Identify the preparation type.
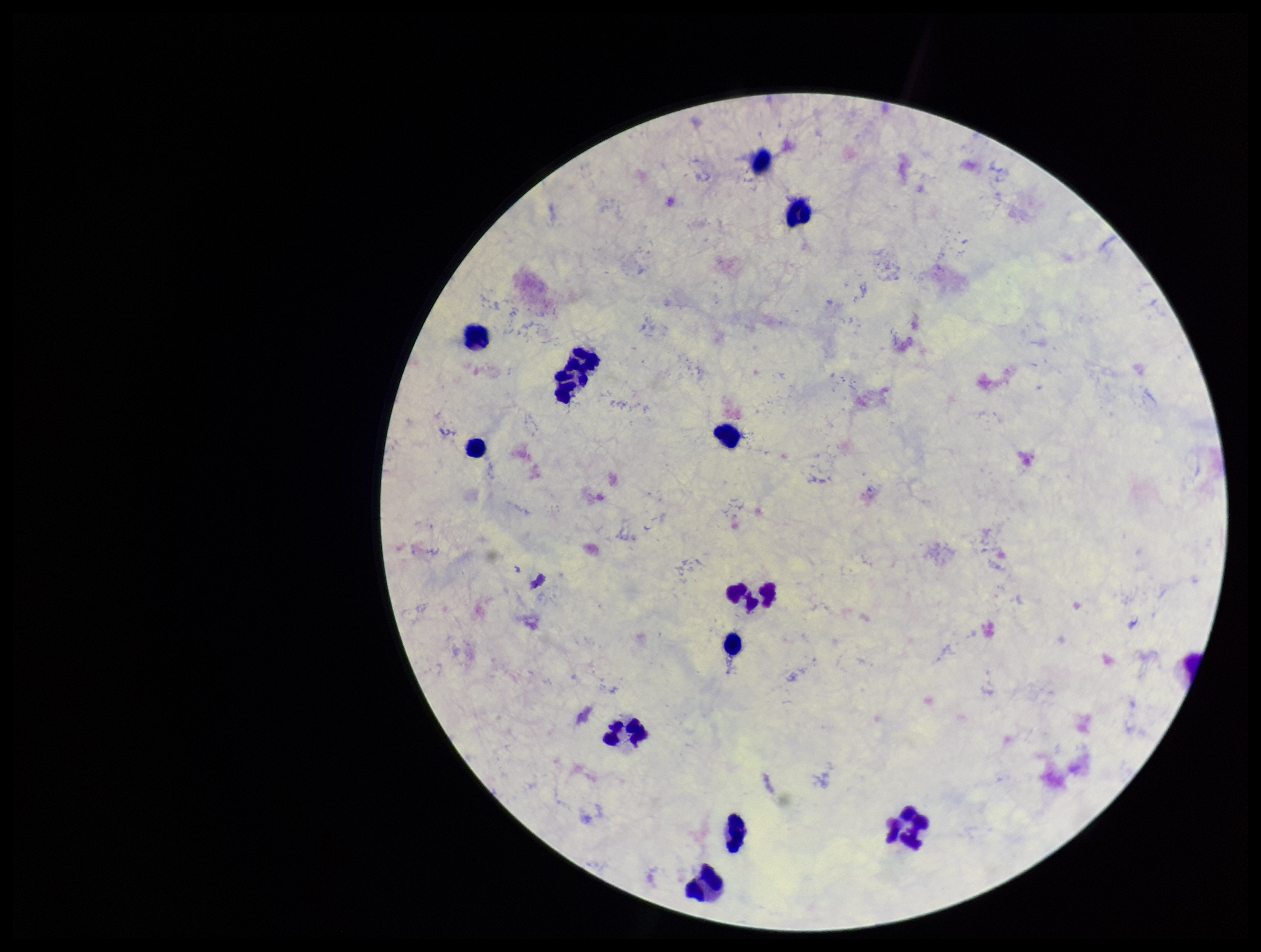
It is a thick blood smear.

Summary:
  - Plasmodium parasites: none seen
  - Capture: smartphone photograph through the microscope eyepiece
  - Stain: Giemsa
  - Field of view: one from this slide
  - Leukocyte count: 13
  - Image size: 1261×952 pixels
  - Parasite count: 0
  - Patient malaria status: negative